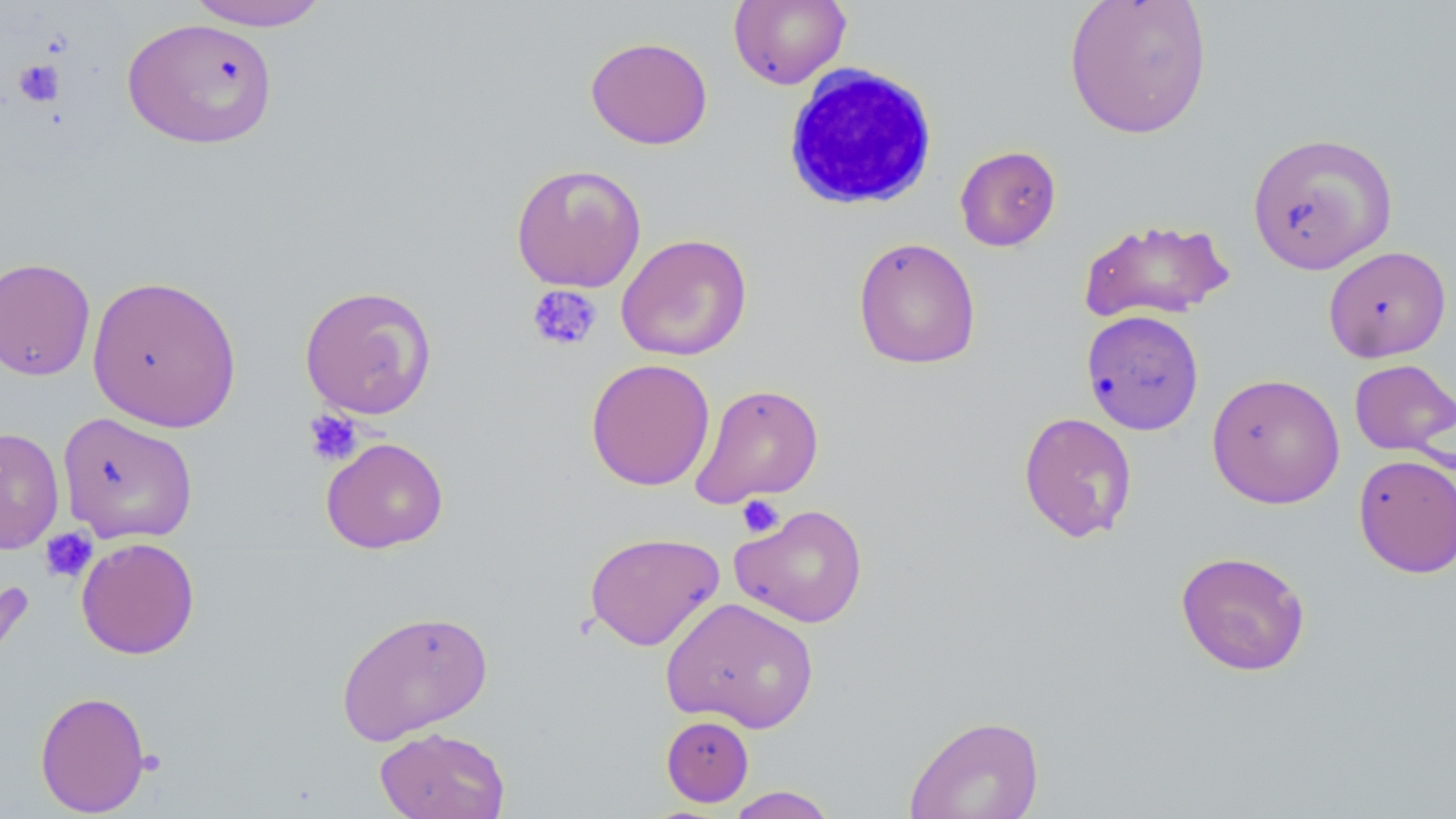

Summary:
  - Coordinate format: approximate bounding boxes as named x1/y1/x2/y2 corners in pixels
  - Uninfected red blood cell locations: (x1=183, y1=0, x2=331, y2=31), (x1=1063, y1=0, x2=1213, y2=140), (x1=728, y1=1, x2=851, y2=89), (x1=122, y1=17, x2=278, y2=148), (x1=585, y1=36, x2=713, y2=150), (x1=1247, y1=131, x2=1398, y2=274), (x1=954, y1=145, x2=1061, y2=251), (x1=510, y1=163, x2=647, y2=292), (x1=1076, y1=217, x2=1236, y2=324), (x1=615, y1=233, x2=753, y2=361), (x1=853, y1=236, x2=981, y2=369), (x1=1323, y1=245, x2=1452, y2=363), (x1=0, y1=257, x2=96, y2=381), (x1=86, y1=274, x2=243, y2=432), (x1=298, y1=284, x2=437, y2=419), (x1=1081, y1=309, x2=1204, y2=435), (x1=585, y1=358, x2=715, y2=491), (x1=1349, y1=358, x2=1455, y2=456), (x1=1206, y1=372, x2=1345, y2=509), (x1=689, y1=383, x2=825, y2=508), (x1=56, y1=411, x2=198, y2=545), (x1=1018, y1=412, x2=1138, y2=543), (x1=0, y1=427, x2=65, y2=555), (x1=321, y1=436, x2=449, y2=554), (x1=1352, y1=452, x2=1456, y2=578), (x1=730, y1=503, x2=868, y2=629), (x1=584, y1=530, x2=725, y2=651), (x1=76, y1=537, x2=200, y2=660), (x1=1175, y1=550, x2=1311, y2=676), (x1=661, y1=597, x2=820, y2=734), (x1=336, y1=608, x2=493, y2=746), (x1=34, y1=690, x2=151, y2=816), (x1=903, y1=714, x2=1045, y2=818), (x1=661, y1=715, x2=754, y2=806), (x1=375, y1=726, x2=510, y2=819), (x1=725, y1=785, x2=838, y2=818)
  - White blood cell locations: (x1=781, y1=63, x2=940, y2=212)
  - Platelet locations: (x1=13, y1=59, x2=65, y2=107), (x1=526, y1=284, x2=603, y2=353), (x1=302, y1=409, x2=363, y2=467), (x1=736, y1=494, x2=785, y2=539), (x1=39, y1=527, x2=97, y2=584), (x1=135, y1=749, x2=166, y2=776)
  - Slide-level diagnosis: negative for blood parasites
  - Modality: light microscopy
  - Field of view: single
  - Stain: May-Grünwald-Giemsa
  - Magnification: 1000x
  - Image size: 1456×819 pixels
  - Preparation: thin blood film